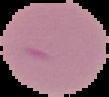

Summary:
  - Image size: 109×97 pixels
  - Image type: segmented cell region with the area outside set to black
  - Malaria status: uninfected
  - Preparation: thin blood film